State which parasite is depicted.
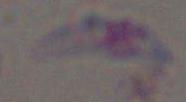

This is Toxoplasma gondii.

Photomicrograph. 1000x magnification.